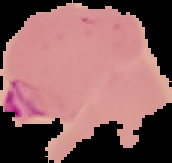
Summary:
  - Image type: segmented cell region on a black background
  - Preparation: thin blood film
  - Image size: 172×163 pixels
  - Result: Plasmodium parasites identified